State which parasite is depicted.
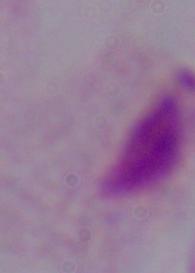

This is a trichomonad.

{
  "modality": "photomicrograph",
  "magnification": "1000x"
}